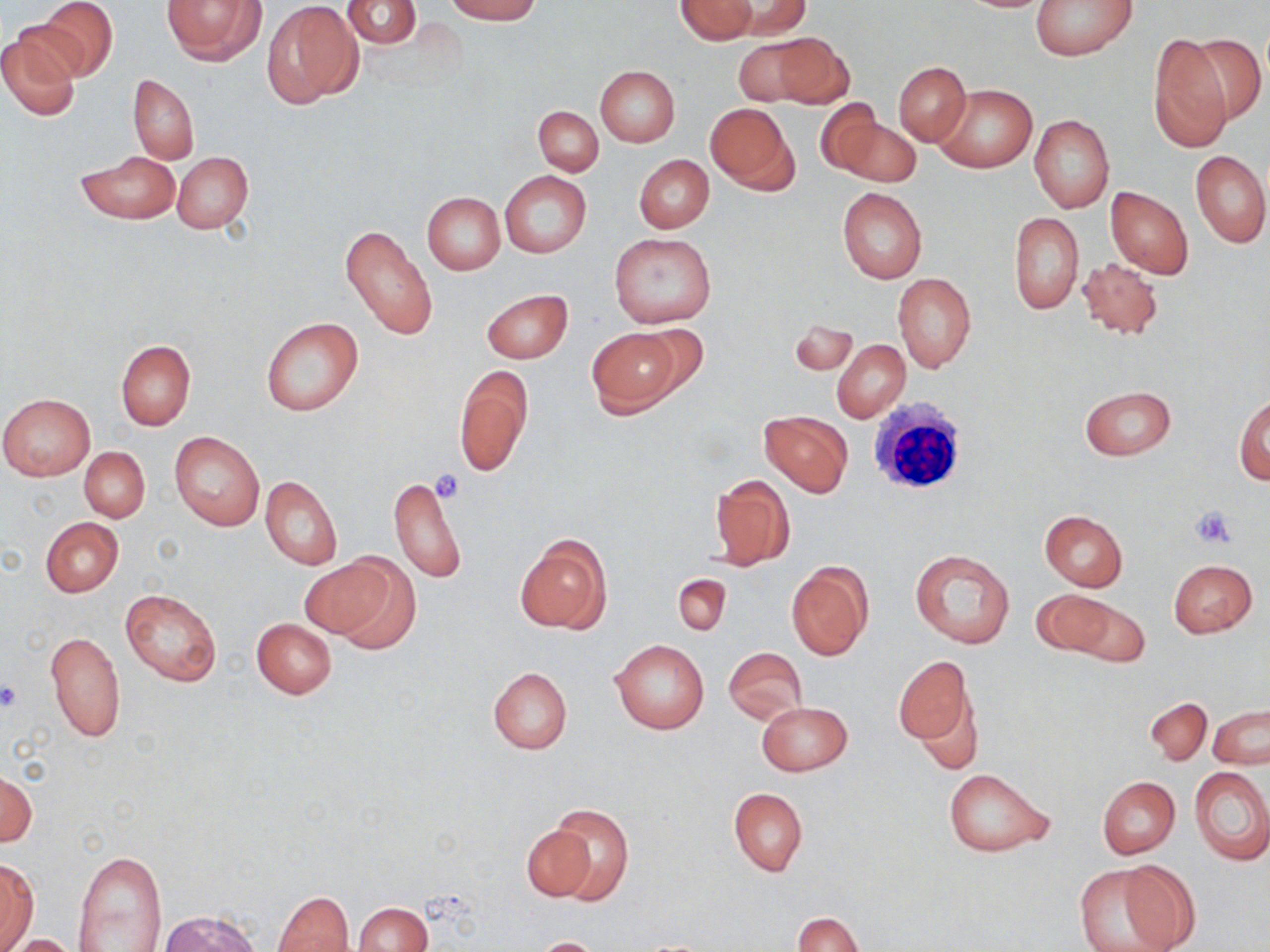

Approximate bounding boxes as named x1/y1/x2/y2 corners in pixels. Platelet locations: (x1=430, y1=470, x2=466, y2=504), (x1=1190, y1=506, x2=1236, y2=549), (x1=0, y1=680, x2=24, y2=714). White blood cell locations: (x1=865, y1=396, x2=972, y2=497). Uninfected red blood cell locations: (x1=37, y1=0, x2=118, y2=81), (x1=161, y1=0, x2=266, y2=65), (x1=262, y1=0, x2=363, y2=109), (x1=342, y1=0, x2=421, y2=48), (x1=446, y1=0, x2=540, y2=23), (x1=675, y1=0, x2=757, y2=44), (x1=724, y1=0, x2=810, y2=39), (x1=1029, y1=0, x2=1137, y2=60), (x1=0, y1=29, x2=82, y2=122), (x1=1190, y1=31, x2=1265, y2=125), (x1=770, y1=32, x2=852, y2=108), (x1=732, y1=35, x2=826, y2=105), (x1=1148, y1=35, x2=1233, y2=152), (x1=894, y1=62, x2=970, y2=145), (x1=596, y1=66, x2=680, y2=147), (x1=128, y1=73, x2=200, y2=165), (x1=937, y1=84, x2=1034, y2=173), (x1=813, y1=99, x2=887, y2=177), (x1=705, y1=103, x2=797, y2=193), (x1=533, y1=107, x2=602, y2=175), (x1=1029, y1=114, x2=1114, y2=213), (x1=837, y1=116, x2=922, y2=187), (x1=1190, y1=149, x2=1269, y2=248), (x1=78, y1=151, x2=180, y2=225), (x1=171, y1=152, x2=253, y2=233), (x1=634, y1=154, x2=714, y2=232), (x1=499, y1=171, x2=590, y2=259), (x1=1106, y1=186, x2=1193, y2=279), (x1=838, y1=188, x2=927, y2=284), (x1=423, y1=192, x2=505, y2=275), (x1=1009, y1=211, x2=1083, y2=314), (x1=340, y1=223, x2=438, y2=342), (x1=608, y1=233, x2=715, y2=327), (x1=1075, y1=257, x2=1164, y2=340), (x1=892, y1=272, x2=976, y2=372), (x1=481, y1=289, x2=573, y2=363), (x1=787, y1=316, x2=858, y2=379), (x1=262, y1=318, x2=364, y2=416), (x1=625, y1=324, x2=711, y2=400), (x1=587, y1=327, x2=681, y2=416), (x1=832, y1=340, x2=910, y2=422), (x1=116, y1=341, x2=195, y2=429), (x1=453, y1=365, x2=532, y2=477), (x1=1080, y1=385, x2=1176, y2=460), (x1=0, y1=394, x2=95, y2=481), (x1=1235, y1=395, x2=1270, y2=485), (x1=758, y1=411, x2=853, y2=497), (x1=171, y1=431, x2=264, y2=531), (x1=79, y1=447, x2=150, y2=523), (x1=389, y1=474, x2=467, y2=584), (x1=708, y1=474, x2=796, y2=570), (x1=260, y1=476, x2=342, y2=570), (x1=1039, y1=510, x2=1128, y2=590), (x1=40, y1=517, x2=124, y2=597), (x1=513, y1=533, x2=611, y2=635), (x1=909, y1=549, x2=1015, y2=649), (x1=300, y1=555, x2=401, y2=644), (x1=1169, y1=559, x2=1257, y2=637), (x1=785, y1=560, x2=874, y2=662), (x1=673, y1=573, x2=730, y2=636), (x1=120, y1=587, x2=221, y2=686), (x1=1031, y1=589, x2=1119, y2=657), (x1=1065, y1=597, x2=1149, y2=668), (x1=251, y1=618, x2=337, y2=699), (x1=45, y1=630, x2=125, y2=743), (x1=611, y1=639, x2=709, y2=734), (x1=723, y1=647, x2=806, y2=723), (x1=893, y1=656, x2=976, y2=754), (x1=487, y1=666, x2=573, y2=755), (x1=1145, y1=698, x2=1211, y2=765), (x1=757, y1=701, x2=852, y2=776), (x1=1209, y1=704, x2=1269, y2=767), (x1=1189, y1=765, x2=1270, y2=865), (x1=0, y1=766, x2=36, y2=850), (x1=942, y1=768, x2=1054, y2=857), (x1=1097, y1=777, x2=1179, y2=858), (x1=728, y1=787, x2=807, y2=876), (x1=545, y1=804, x2=634, y2=905), (x1=520, y1=821, x2=601, y2=902), (x1=74, y1=848, x2=169, y2=952), (x1=0, y1=860, x2=39, y2=951), (x1=1075, y1=862, x2=1187, y2=952), (x1=271, y1=890, x2=355, y2=952), (x1=353, y1=902, x2=431, y2=952), (x1=155, y1=912, x2=266, y2=952), (x1=792, y1=912, x2=863, y2=952), (x1=5, y1=935, x2=84, y2=952), (x1=531, y1=937, x2=609, y2=951). Slide-level diagnosis: negative for blood parasites. Light microscopy. Single field of view. 1000x magnification. Thin blood film. Image is 1270×952 pixels. May-Grünwald-Giemsa-stained preparation.